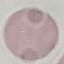

Result: no malaria parasites seen. Photographed with a smartphone camera at the microscope eyepiece. Giemsa-stained preparation. Cell patch, automatically extracted from a larger field of view and resized to 64 × 64 pixels. Thin blood film.